Point out each malaria parasite.
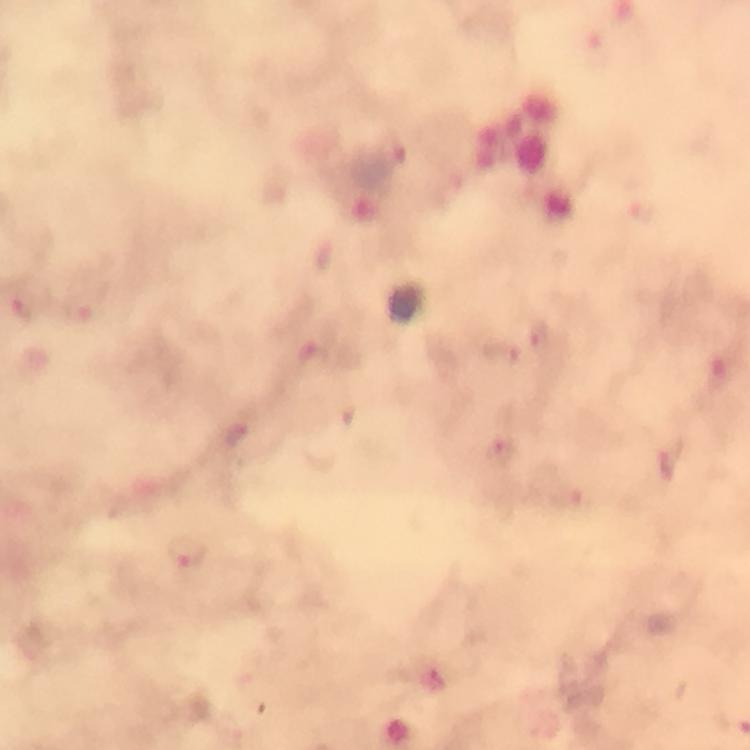
Approximate centers as {x, y} in pixels.
Malaria parasites: {25, 304}, {541, 340}, {500, 351}, {314, 360}, {237, 434}, {502, 452}, {667, 466}, {185, 556}, {434, 681}.

Summary:
  - Image size: 750×750 pixels
  - Context: from a diagnostic examination for malaria
  - Cropped from: a single field of view
  - Magnification: 100x
  - Preparation: thick blood smear
  - Immersion oil: applied
  - Stain: Giemsa
  - Capture: smartphone photograph through a microscope